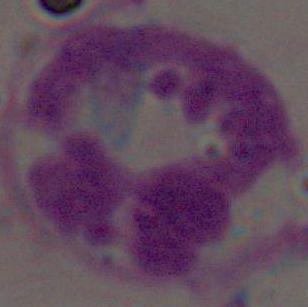

Photomicrograph. 1000x magnification. A white blood cell is shown.